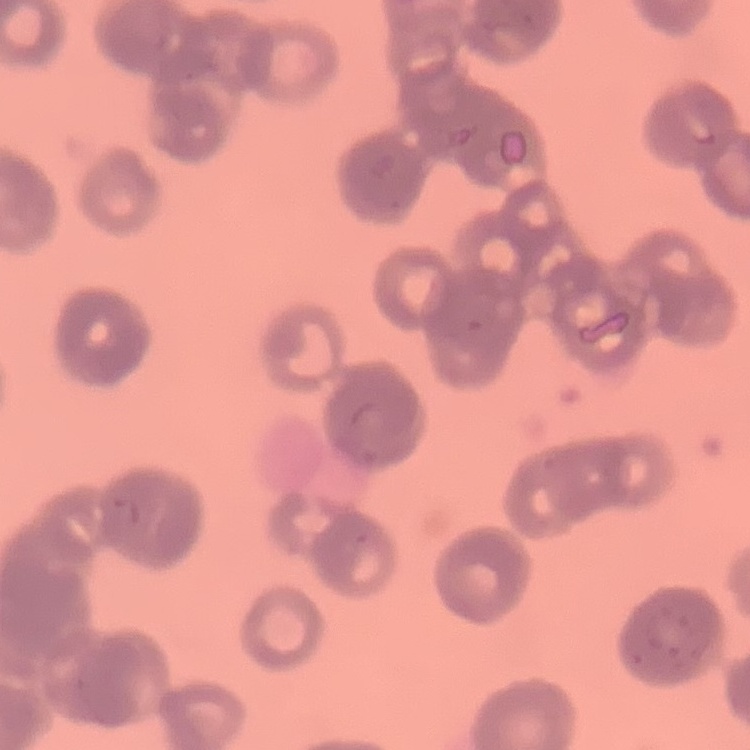
{
  "erythrocyte_morphology": "rouleaux formation",
  "preparation": "thin peripheral smear",
  "image_type": "square crop of a larger photomicrograph",
  "stain": "Field's or Giemsa"
}